Locate platelets.
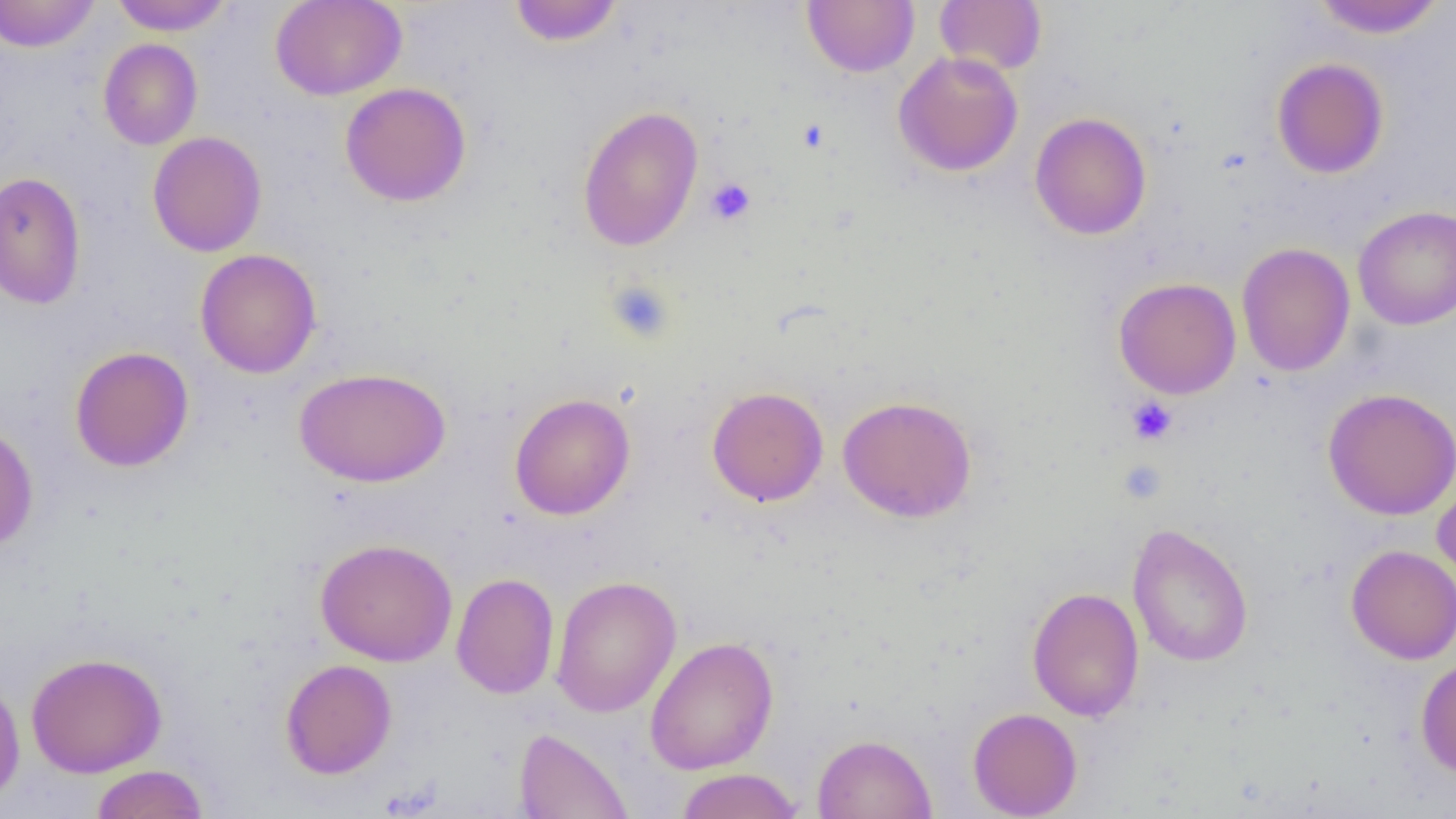

Approximate bounding boxes as (x1,y1)-(x2,y2) corner pairs in pixels.
Platelets: (705,178)-(755,225), (605,279)-(675,342), (1126,396)-(1177,445), (1117,460)-(1167,504).

slide-level diagnosis = no evidence of blood parasites
field of view = single
uninfected red blood cell locations = approximate bounding boxes as (x1,y1)-(x2,y2) corner pairs in pixels: (0,0)-(100,52), (110,0)-(233,35), (270,0)-(407,101), (1311,0)-(1446,38), (509,1)-(622,47), (803,1)-(919,77), (934,1)-(1047,76), (98,38)-(202,150), (894,51)-(1023,176), (1271,58)-(1389,179), (339,82)-(472,207), (577,105)-(704,251), (1030,112)-(1151,240), (148,131)-(267,257), (0,172)-(86,309), (1352,205)-(1456,330), (1236,243)-(1355,376), (194,248)-(322,378), (1114,277)-(1241,399), (69,346)-(194,472), (294,367)-(450,487), (707,386)-(829,506), (1323,388)-(1456,520), (509,393)-(635,520), (837,395)-(977,523), (0,423)-(39,551), (1432,473)-(1456,590), (1126,522)-(1254,668), (315,538)-(457,666), (1346,545)-(1456,664), (451,573)-(558,699), (550,575)-(682,718), (1027,586)-(1144,722), (645,636)-(779,775), (25,652)-(167,778), (1415,657)-(1456,778), (280,659)-(397,779), (0,675)-(26,805), (967,707)-(1083,818), (513,727)-(634,819), (812,733)-(937,818), (89,764)-(210,819), (674,768)-(804,819)
image size = 1456×819 pixels
modality = light microscopy
preparation = thin blood smear
magnification = 1000x